State the blood parasite species.
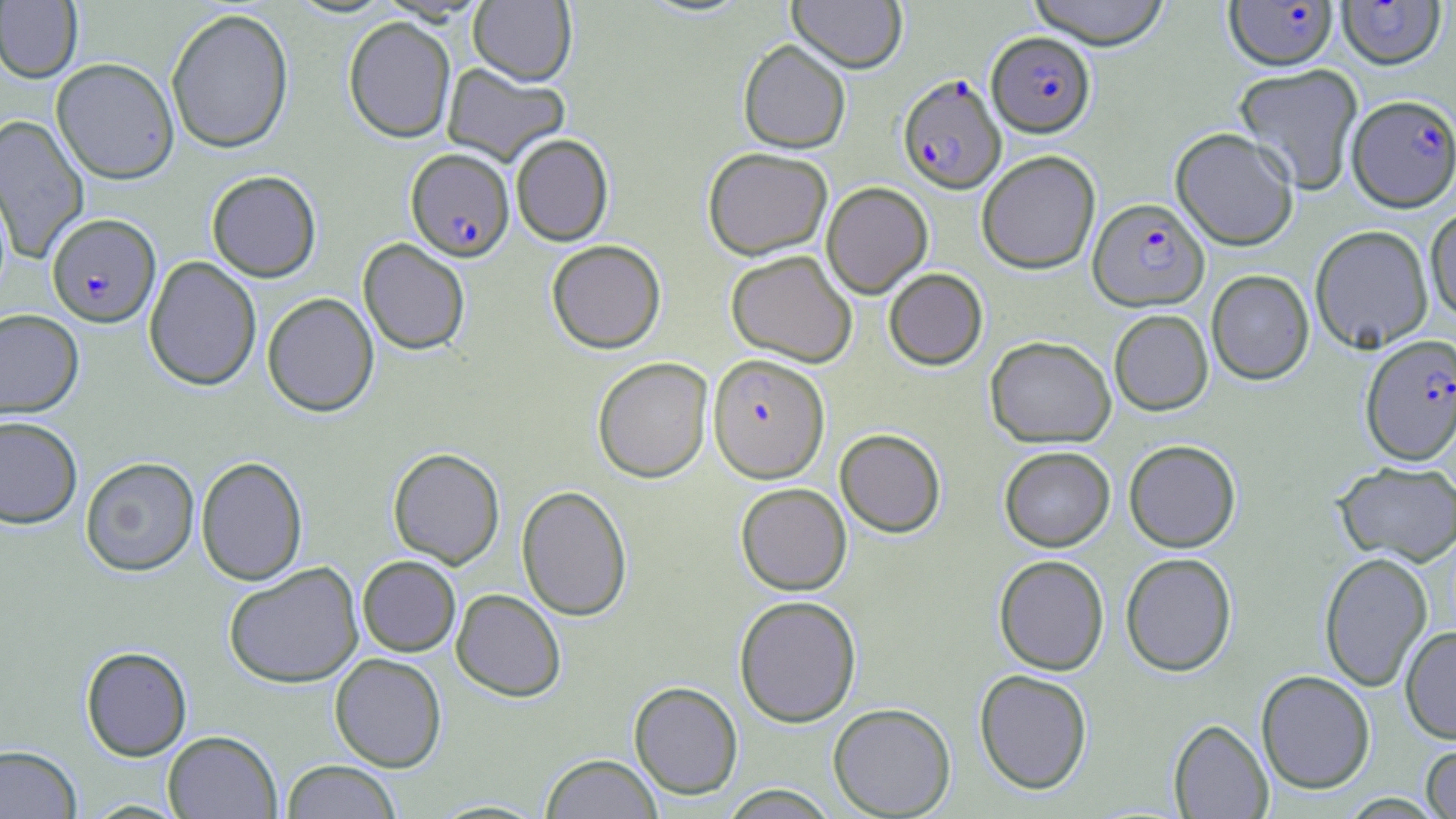
Plasmodium falciparum.

Summary:
  - Coordinate format: approximate bounding boxes as [x1, y1, x2, y2] in pixels
  - Uninfected red blood cell locations: [788, 0, 907, 73], [1026, 0, 1172, 48], [0, 1, 83, 83], [468, 1, 577, 85], [166, 7, 294, 154], [343, 16, 456, 143], [738, 39, 851, 153], [51, 57, 179, 184], [442, 63, 569, 166], [1233, 63, 1364, 194], [0, 114, 90, 265], [1170, 127, 1299, 250], [511, 133, 613, 246], [702, 146, 833, 260], [977, 150, 1101, 274], [206, 170, 321, 282], [821, 182, 933, 298], [1425, 206, 1456, 322], [1310, 224, 1433, 353], [358, 238, 470, 354], [547, 239, 666, 353], [725, 250, 857, 367], [144, 256, 262, 391], [883, 268, 988, 370], [1206, 270, 1314, 384], [262, 292, 379, 416], [0, 309, 84, 419], [1109, 309, 1213, 415], [985, 336, 1116, 448], [592, 356, 713, 483], [0, 415, 83, 529], [835, 428, 946, 537], [1124, 439, 1240, 552], [999, 446, 1115, 551], [388, 447, 505, 569], [80, 456, 200, 576], [196, 456, 308, 586], [1334, 460, 1456, 566], [735, 483, 851, 595], [516, 485, 632, 621], [1319, 551, 1432, 691], [1120, 552, 1237, 676], [994, 554, 1109, 675], [357, 555, 460, 656], [224, 562, 364, 688], [451, 589, 566, 701], [734, 595, 861, 727], [1400, 625, 1456, 744], [80, 646, 192, 760], [329, 653, 447, 772], [974, 669, 1093, 794], [1256, 670, 1376, 794], [628, 681, 743, 799], [828, 702, 956, 818], [1168, 719, 1273, 819], [163, 730, 282, 818], [1421, 742, 1456, 819], [0, 744, 82, 818], [540, 753, 663, 818], [280, 760, 401, 819], [719, 785, 841, 818], [80, 799, 191, 818]
  - Plasmodium falciparum-infected red blood cell locations: [1225, 1, 1338, 70], [1337, 1, 1446, 69], [987, 31, 1095, 137], [898, 74, 1006, 194], [1347, 94, 1456, 211], [405, 148, 514, 261], [1088, 197, 1209, 310], [47, 213, 161, 327], [1360, 333, 1456, 465], [708, 353, 830, 483]
  - Image size: 1456×819 pixels
  - Field of view: single
  - Modality: light microscopy
  - Preparation: thin blood film
  - Stain: May-Grünwald-Giemsa
  - Magnification: 1000x